Identify the cell.
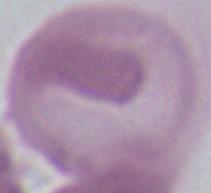
This is an erythrocyte.

Micrograph. Captured at 1000x magnification.